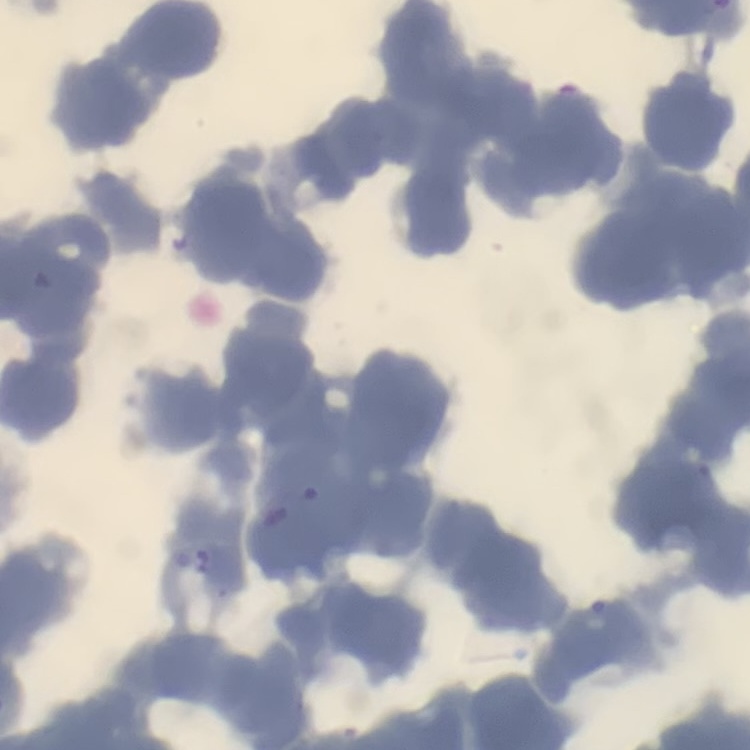 The erythrocytes show rouleaux formation. Stained with either Field's or Giemsa. Thin blood smear. One tile cut from a larger photomicrograph.